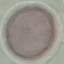

Result: negative for malaria parasites. Photographed with a smartphone camera at the microscope eyepiece. Cell patch, automatically extracted from a larger field of view and resized to 64 × 64 pixels. Giemsa-stained preparation. Thin blood smear.